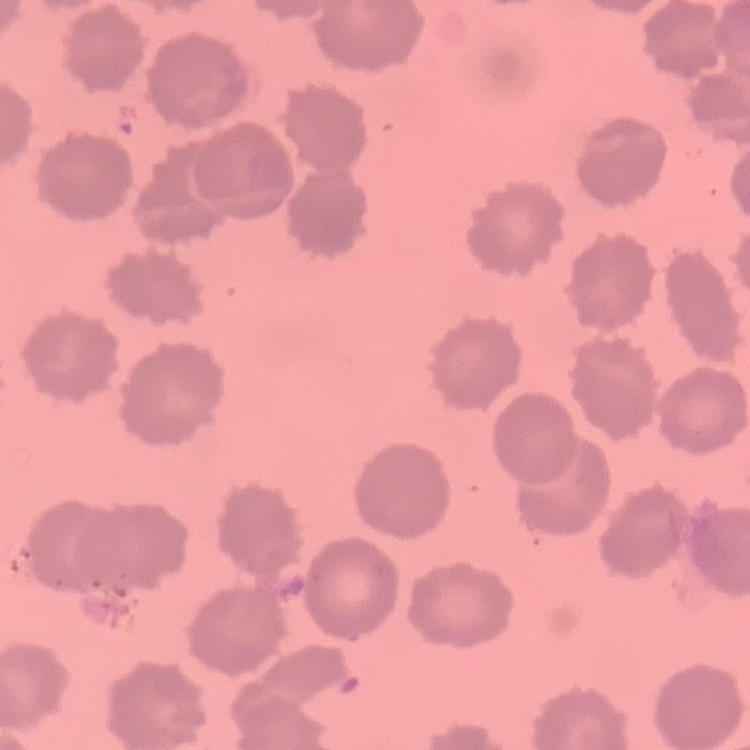

erythrocyte_morphology: no rouleaux formation
image_type: square crop of a larger photomicrograph
stain: Field's or Giemsa
preparation: thin blood smear